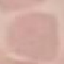
Result: no malaria parasites seen. Thin smear of blood. Cell patch, automatically extracted from a larger field of view and resized to 64 × 64 pixels. Giemsa stain. Acquired by smartphone through the microscope eyepiece.